Identify the blood parasite species.
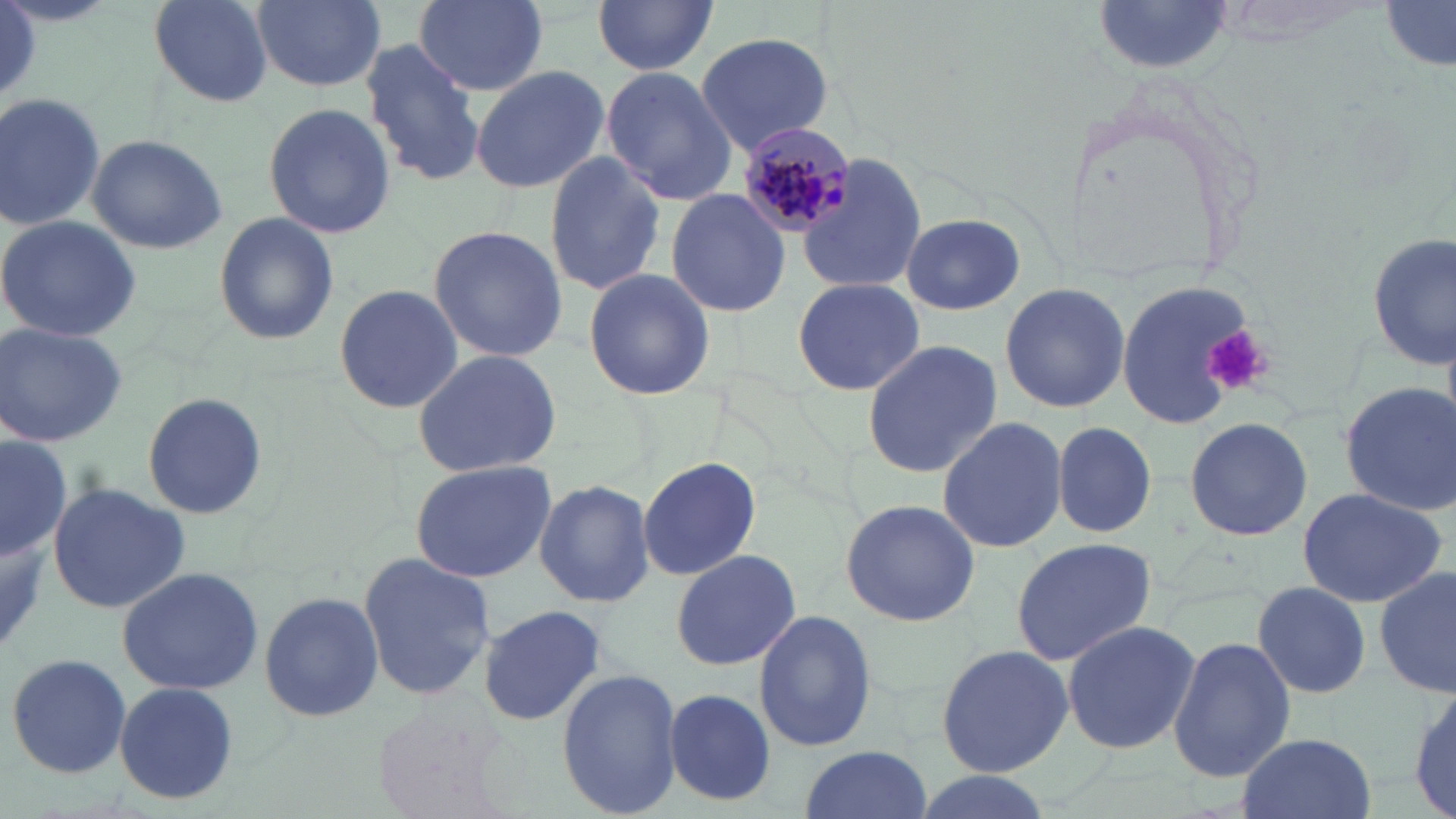
Plasmodium malariae.

Summary:
  - Coordinate format: approximate bounding boxes as named x1/y1/x2/y2 corners in pixels
  - Uninfected red blood cell locations: (x1=148, y1=0, x2=275, y2=106), (x1=250, y1=0, x2=387, y2=94), (x1=413, y1=0, x2=550, y2=97), (x1=594, y1=0, x2=719, y2=76), (x1=1381, y1=1, x2=1454, y2=69), (x1=1095, y1=3, x2=1239, y2=77), (x1=695, y1=31, x2=835, y2=153), (x1=360, y1=39, x2=484, y2=185), (x1=470, y1=64, x2=609, y2=194), (x1=601, y1=64, x2=738, y2=207), (x1=0, y1=93, x2=105, y2=232), (x1=262, y1=101, x2=398, y2=240), (x1=85, y1=133, x2=228, y2=254), (x1=544, y1=153, x2=665, y2=293), (x1=797, y1=153, x2=926, y2=295), (x1=666, y1=189, x2=793, y2=318), (x1=213, y1=211, x2=339, y2=346), (x1=0, y1=214, x2=142, y2=342), (x1=901, y1=215, x2=1025, y2=315), (x1=428, y1=225, x2=568, y2=361), (x1=1366, y1=235, x2=1453, y2=371), (x1=582, y1=268, x2=715, y2=399), (x1=1112, y1=276, x2=1263, y2=427), (x1=793, y1=277, x2=923, y2=394), (x1=999, y1=282, x2=1130, y2=414), (x1=332, y1=284, x2=466, y2=413), (x1=0, y1=322, x2=129, y2=449), (x1=863, y1=339, x2=1001, y2=477), (x1=411, y1=348, x2=561, y2=478), (x1=1341, y1=380, x2=1455, y2=513), (x1=141, y1=393, x2=269, y2=520), (x1=937, y1=416, x2=1067, y2=554), (x1=1183, y1=417, x2=1313, y2=540), (x1=1051, y1=420, x2=1157, y2=537), (x1=0, y1=437, x2=71, y2=560), (x1=409, y1=458, x2=556, y2=582), (x1=637, y1=458, x2=762, y2=581), (x1=534, y1=478, x2=654, y2=608), (x1=46, y1=481, x2=189, y2=613), (x1=1296, y1=486, x2=1448, y2=609), (x1=839, y1=496, x2=983, y2=627), (x1=1009, y1=537, x2=1158, y2=665), (x1=669, y1=547, x2=802, y2=671), (x1=358, y1=552, x2=497, y2=699), (x1=116, y1=565, x2=264, y2=695), (x1=1375, y1=565, x2=1455, y2=699), (x1=1251, y1=580, x2=1373, y2=700), (x1=258, y1=591, x2=384, y2=724), (x1=476, y1=603, x2=607, y2=727), (x1=752, y1=608, x2=878, y2=754), (x1=1060, y1=619, x2=1200, y2=756), (x1=1167, y1=634, x2=1297, y2=782), (x1=935, y1=643, x2=1073, y2=779), (x1=6, y1=650, x2=131, y2=779), (x1=556, y1=668, x2=682, y2=817), (x1=112, y1=681, x2=240, y2=805), (x1=1408, y1=682, x2=1456, y2=819), (x1=663, y1=689, x2=773, y2=805), (x1=371, y1=702, x2=507, y2=819), (x1=1236, y1=732, x2=1378, y2=819), (x1=798, y1=745, x2=933, y2=819), (x1=903, y1=773, x2=1056, y2=819)
  - Platelet locations: (x1=1205, y1=324, x2=1270, y2=396)
  - Plasmodium malariae-infected red blood cell locations: (x1=731, y1=122, x2=860, y2=236)
  - Stain: May-Grünwald-Giemsa
  - Modality: optical microscopy
  - Preparation: thin blood film
  - Field of view: one of a larger specimen
  - Magnification: 1000x
  - Image size: 1456×819 pixels